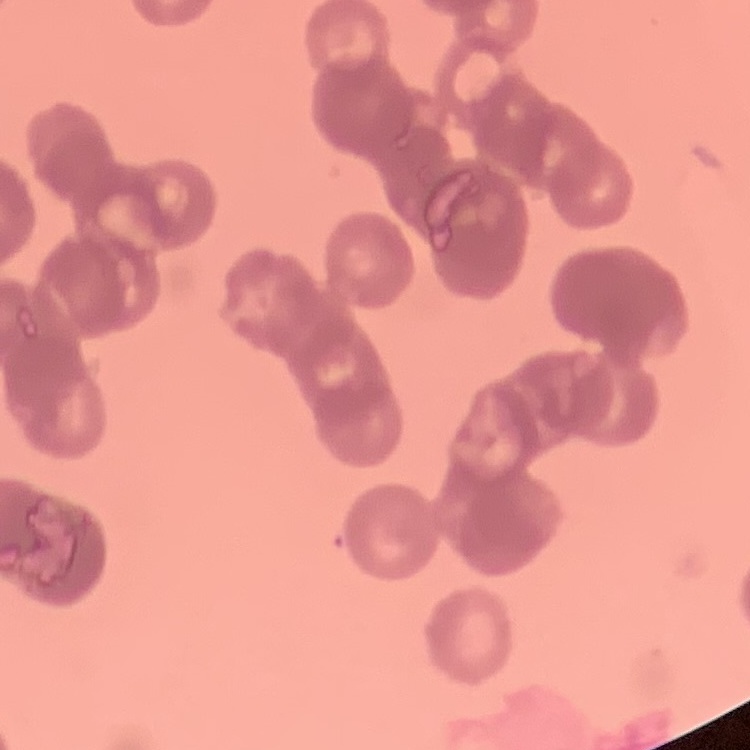 The erythrocytes exhibit rouleaux formation. Stained with either Field's or Giemsa. Thin peripheral smear. One tile cut from a larger photomicrograph.